Report the malaria status.
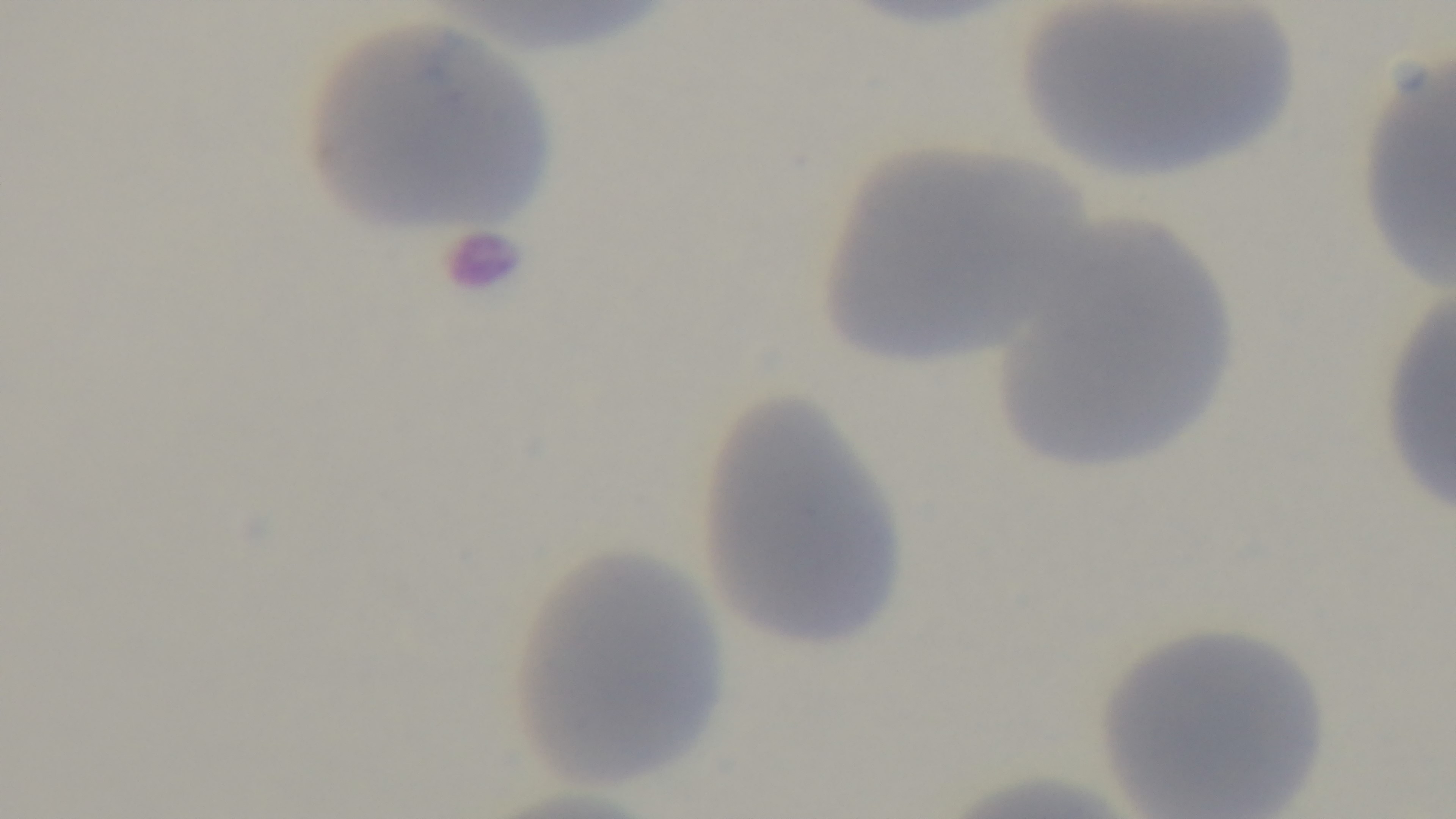

Uninfected.

Summary:
  - Preparation: thin smear
  - Capture: mounted 4K digital camera
  - Modality: light microscopy
  - Field of view: one from the slide
  - Stain: Giemsa
  - Objective: 100x oil immersion